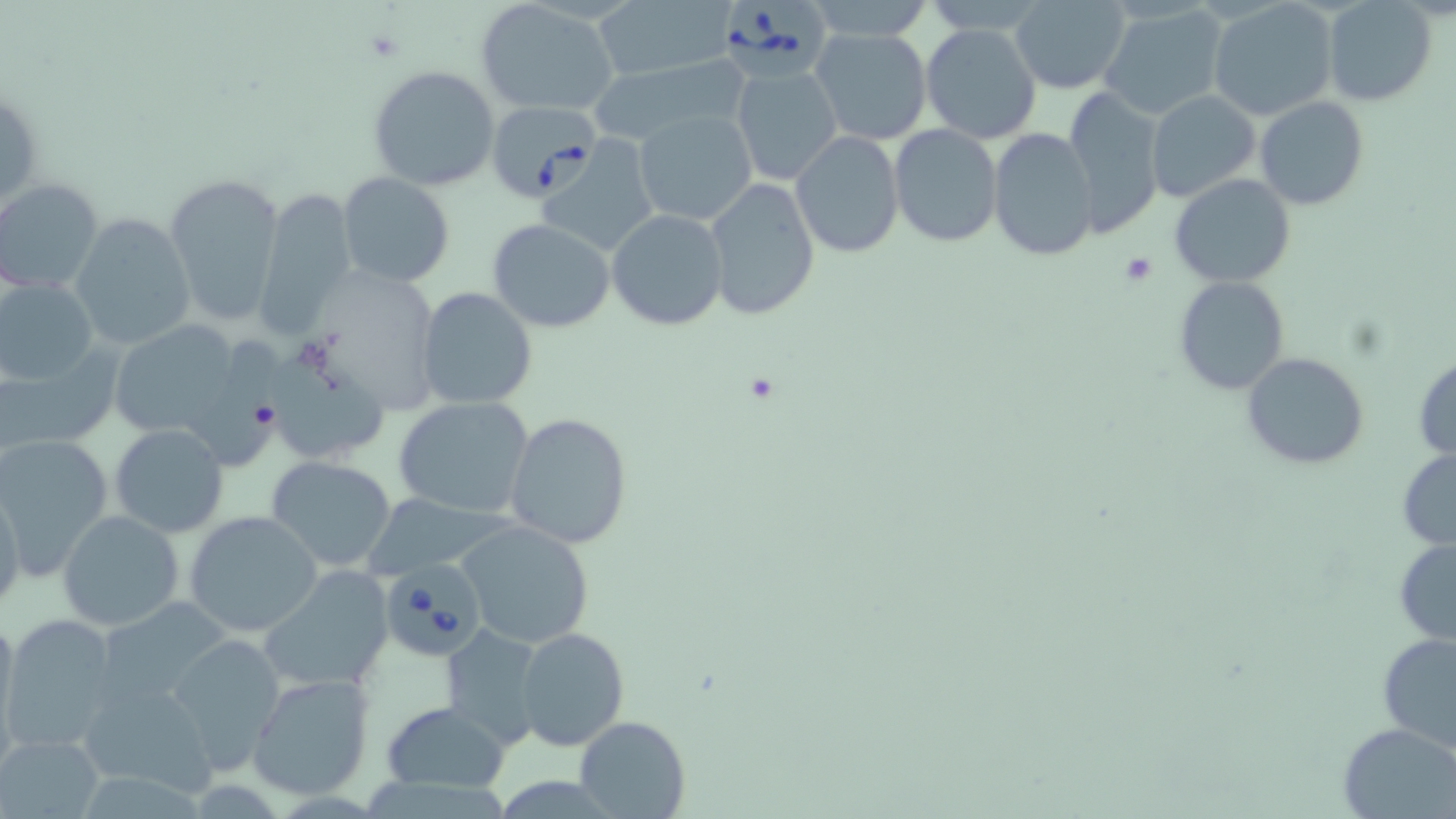 Approximate bounding boxes as [x1, y1, x2, y2] in pixels. Uninfected red blood cell locations: [475, 0, 620, 118], [800, 0, 934, 41], [591, 1, 735, 85], [1008, 1, 1132, 92], [1208, 1, 1338, 122], [1321, 1, 1437, 106], [1097, 3, 1228, 121], [922, 22, 1041, 145], [807, 27, 933, 147], [592, 53, 750, 146], [368, 66, 500, 192], [732, 66, 842, 187], [1064, 88, 1167, 239], [1146, 89, 1262, 205], [1253, 95, 1370, 210], [634, 109, 757, 227], [889, 124, 1003, 248], [988, 127, 1097, 262], [790, 131, 905, 259], [537, 139, 663, 257], [164, 171, 287, 328], [337, 173, 455, 289], [1170, 174, 1296, 289], [702, 177, 822, 320], [0, 178, 104, 294], [254, 184, 359, 339], [607, 209, 728, 330], [70, 215, 194, 351], [486, 219, 616, 333], [1174, 275, 1290, 395], [1, 277, 99, 386], [416, 287, 539, 410], [105, 318, 247, 447], [192, 336, 289, 475], [0, 343, 123, 457], [266, 352, 389, 460], [1242, 352, 1369, 471], [1413, 355, 1456, 461], [393, 397, 533, 519], [505, 412, 633, 551], [108, 423, 229, 538], [0, 434, 115, 577], [1398, 447, 1455, 551], [265, 454, 400, 573], [0, 484, 24, 618], [58, 510, 185, 629], [185, 511, 323, 637], [457, 520, 597, 648], [1393, 538, 1456, 647], [257, 567, 396, 694], [96, 598, 233, 710], [0, 609, 20, 742], [1, 614, 120, 754], [442, 624, 546, 750], [514, 627, 628, 749], [164, 631, 287, 774], [1375, 633, 1456, 754], [246, 673, 375, 801], [78, 676, 219, 798], [382, 701, 511, 793], [575, 715, 689, 819], [1338, 720, 1455, 818], [3, 734, 103, 815]. Platelet locations: [1122, 252, 1158, 286]. Babesia divergens-infected red blood cell locations: [717, 0, 831, 85], [487, 100, 599, 202], [384, 565, 479, 654]. Slide-level diagnosis: Babesia divergens. Thin blood film. Optical microscopy. Captured at 1000x magnification. One field of a larger specimen. Image is 1456×819 pixels. May-Grünwald-Giemsa stain.